Classify this cell by malaria status.
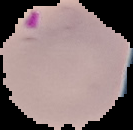
Parasitized.

{
  "preparation": "thin blood film",
  "image_size": "133×130 pixels",
  "image_type": "cell region segmented out of the field of view; surrounding area masked to black"
}